Classify this cell by malaria status.
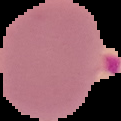

Parasitized.

Summary:
  - Image type: segmented cell region on a black background
  - Image size: 121×121 pixels
  - Preparation: thin blood film